Report the malaria status of this cell.
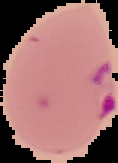

Parasitized.

Summary:
  - Image type: segmented cell region with the area outside set to black
  - Preparation: thin blood smear
  - Image size: 118×163 pixels